Name the cell type shown.
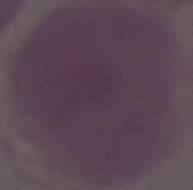
An erythrocyte.

Captured at 1000x magnification. Micrograph.